Describe the morphology of the erythrocytes.
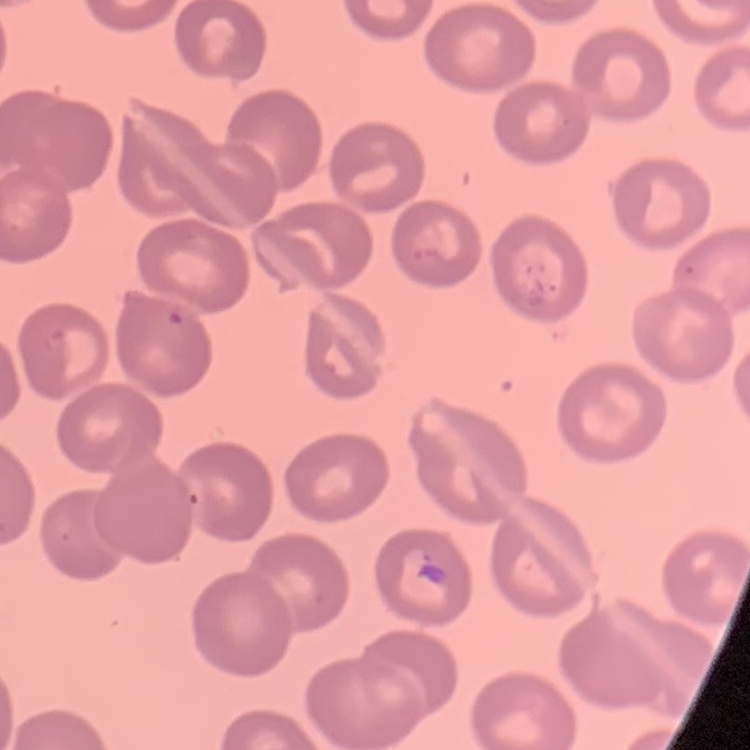
No rouleaux formation.

preparation = thin peripheral smear
image type = one tile cut from a larger photomicrograph
stain = Field's or Giemsa